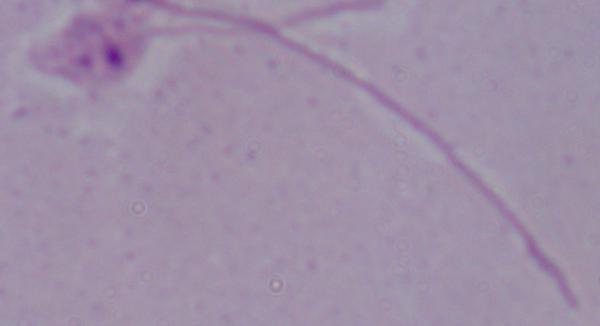

1000x magnification. A Leishmania parasite is seen. Photomicrograph.